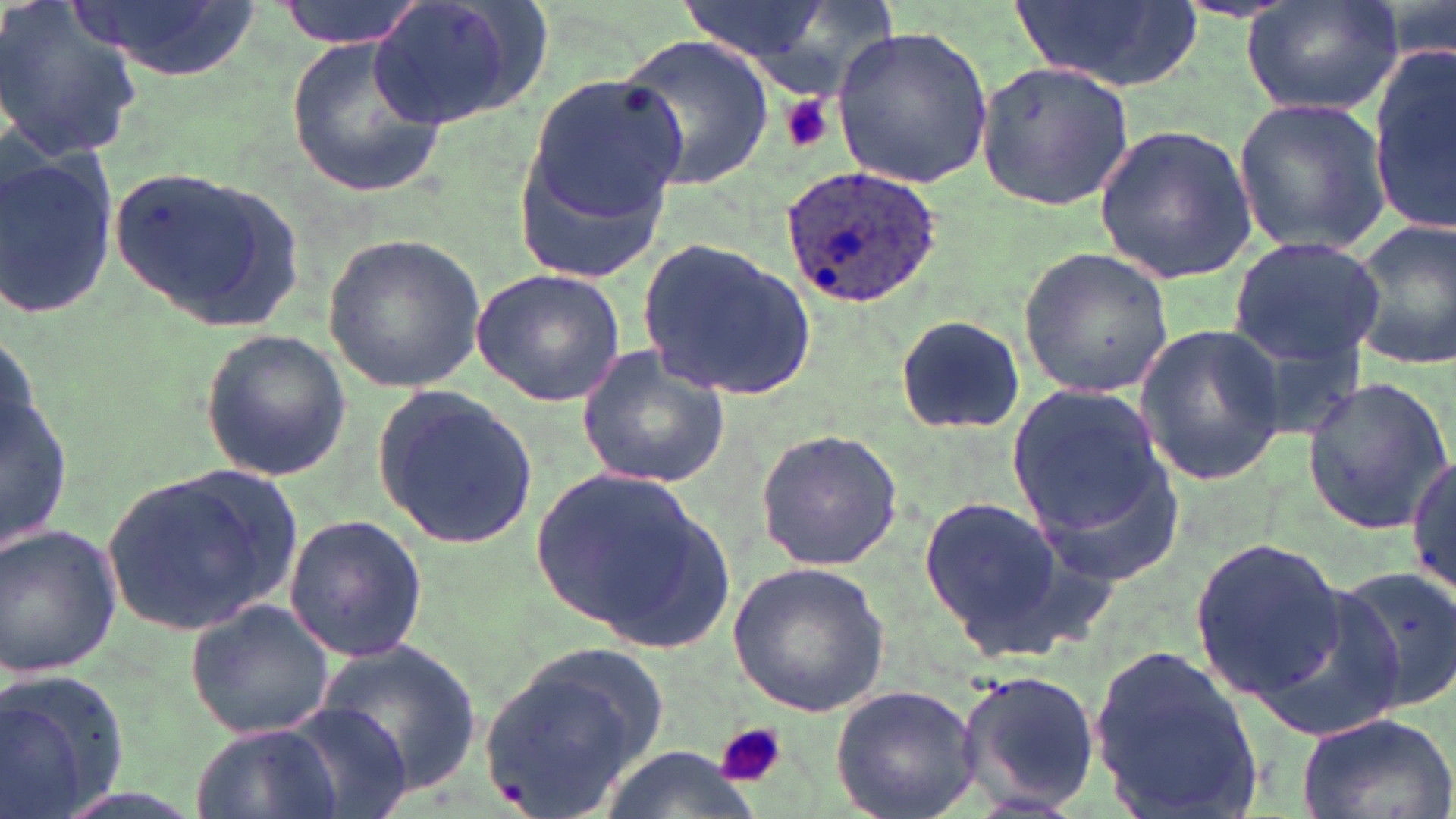
Approximate bounding boxes as (x1,y1)-(x2,y2) corner pairs in pixels. Plasmodium ovale-infected red blood cell locations: (779,163)-(948,310). Uninfected red blood cell locations: (0,0)-(146,161), (75,0)-(262,81), (275,0)-(427,48), (357,0)-(544,135), (1242,0)-(1402,118), (1014,1)-(1202,91), (674,2)-(841,64), (831,24)-(994,190), (617,33)-(774,189), (289,34)-(450,196), (1372,44)-(1455,230), (977,57)-(1136,211), (516,71)-(688,265), (1233,96)-(1393,255), (1093,123)-(1257,282), (0,147)-(117,322), (107,165)-(309,337), (1346,218)-(1456,371), (323,232)-(486,393), (1228,234)-(1386,371), (635,235)-(817,400), (1018,246)-(1175,398), (470,267)-(630,407), (895,311)-(1027,436), (0,322)-(77,576), (1134,322)-(1287,486), (198,328)-(351,483), (575,343)-(733,489), (1299,376)-(1454,534), (373,385)-(539,554), (1006,386)-(1170,539), (752,427)-(904,572), (1019,438)-(1183,589), (1407,456)-(1456,598), (529,463)-(717,640), (102,466)-(306,637), (916,498)-(1067,650), (282,512)-(427,663), (0,523)-(124,680), (1189,536)-(1348,700), (728,561)-(891,717), (1329,565)-(1456,717), (187,598)-(338,740), (314,642)-(483,793), (1092,643)-(1263,819), (477,645)-(673,814), (952,667)-(1101,811), (0,669)-(131,819), (829,683)-(982,819), (284,704)-(414,819), (1293,712)-(1454,819), (192,723)-(345,819), (600,745)-(755,819). Platelet locations: (782,95)-(832,152), (713,721)-(786,790). Slide-level diagnosis: Plasmodium ovale. May-Grünwald-Giemsa stain. Thin blood film. Optical microscopy. Image is 1456×819 pixels. One field of a larger specimen. Captured at 1000x magnification.